Assess the morphology of the erythrocytes.
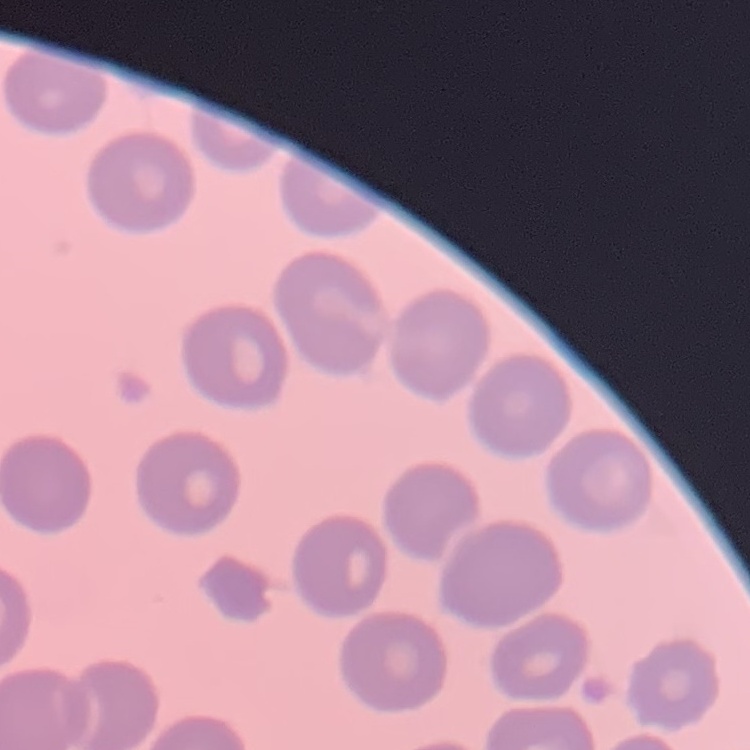
No rouleaux formation.

stain = Field's or Giemsa
image type = square crop of a larger photomicrograph
preparation = thin blood film